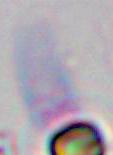
magnification = 1000x
modality = photomicrograph
identification = Toxoplasma gondii